Assess this cell for malaria.
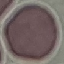
Uninfected.

{
  "preparation": "thin blood film",
  "image_type": "cell patch, automatically extracted from a larger field of view and resized to 64 × 64 pixels",
  "capture": "smartphone camera at the microscope eyepiece",
  "stain": "Giemsa"
}